Give the extent of all Plasmodium vivax-infected red blood cells.
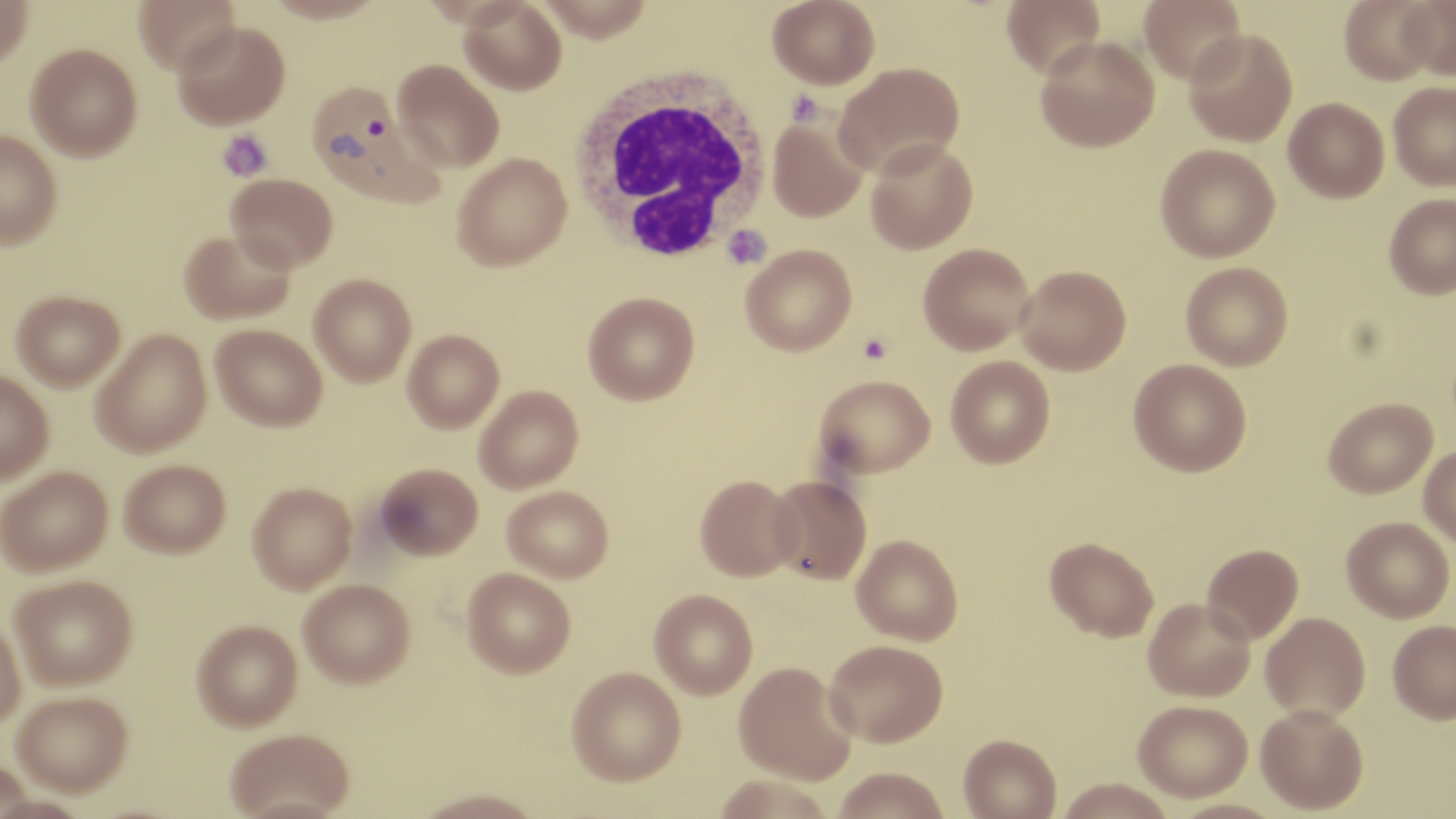
Approximate bounding boxes as (x1,y1)-(x2,y2) corner pairs in pixels.
Plasmodium vivax-infected red blood cells: (308,82)-(449,208).

slide_level_diagnosis: Plasmodium vivax
field_of_view: one of a larger specimen
preparation: thin blood film
white_blood_cell_locations: 'approximate bounding boxes as (x1,y1)-(x2,y2) corner pairs in pixels: (566,67)-(772,265)'
uninfected_red_blood_cell_locations: 'approximate bounding boxes as (x1,y1)-(x2,y2) corner pairs in pixels: (0,0)-(32,71), (133,0)-(240,74), (264,0)-(387,23), (418,0)-(537,29), (534,0)-(654,43), (768,0)-(880,89), (1001,0)-(1105,79), (1139,0)-(1246,85), (1339,0)-(1439,84), (1398,0)-(1456,80), (459,1)-(567,95), (173,22)-(290,130), (1183,28)-(1298,146), (1035,36)-(1160,152), (26,44)-(142,160), (393,59)-(505,172), (833,61)-(966,178), (1388,81)-(1456,190), (1284,98)-(1389,202), (766,110)-(869,223), (0,131)-(62,249), (866,138)-(978,253), (1155,143)-(1280,262), (452,153)-(571,271), (227,173)-(337,272), (1383,194)-(1456,298), (179,228)-(295,324), (918,243)-(1035,354), (740,244)-(857,355), (1181,262)-(1294,370), (1016,265)-(1131,374), (309,273)-(417,386), (11,291)-(125,390), (583,291)-(700,405), (210,324)-(327,431), (91,328)-(211,457), (402,329)-(504,432), (946,356)-(1055,468), (1128,359)-(1251,476), (0,370)-(54,484), (814,374)-(935,477), (474,385)-(584,493), (1323,397)-(1437,498), (1418,445)-(1456,547), (119,459)-(230,557), (375,463)-(482,561), (1,466)-(113,576), (695,474)-(801,580), (767,474)-(873,584), (247,482)-(357,594), (502,486)-(613,582), (1341,516)-(1454,622), (851,534)-(963,645), (1044,537)-(1159,642), (1202,543)-(1304,643), (461,567)-(575,679), (10,574)-(137,691), (299,581)-(415,690), (649,589)-(758,699), (1143,597)-(1255,702), (1260,612)-(1370,722), (0,619)-(26,732), (1388,620)-(1456,724), (191,621)-(303,734), (824,639)-(948,746), (734,662)-(856,785), (567,667)-(687,786), (12,694)-(133,798), (1132,700)-(1252,801), (1255,705)-(1368,815), (224,730)-(354,819), (958,735)-(1062,819), (833,768)-(950,819), (1056,779)-(1175,819), (1167,799)-(1287,819)'
stain: May-Grünwald-Giemsa
modality: optical microscopy
image_size: 1456×819 pixels
magnification: 1000x
platelet_locations: 'approximate bounding boxes as (x1,y1)-(x2,y2) corner pairs in pixels: (785,89)-(825,126), (218,130)-(273,181), (722,225)-(771,270), (859,333)-(892,365)'